Classify this cell by malaria status.
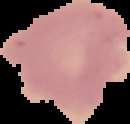
Uninfected.

Summary:
  - Image type: cell region segmented out of the field of view; surrounding area masked to black
  - Image size: 130×124 pixels
  - Preparation: thin blood film